Classify this cell by malaria status.
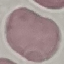
It is uninfected.

Cell patch, automatically extracted from a larger field of view and resized to 64 × 64 pixels. Photographed with a smartphone camera at the microscope eyepiece. Thin blood smear. Giemsa-stained preparation.